Assess this cell for malaria.
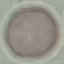
It is uninfected.

{
  "stain": "Giemsa",
  "preparation": "thin smear",
  "capture": "smartphone camera at the microscope eyepiece",
  "image_type": "automatically extracted cell patch, resized to 64 × 64 pixels"
}